Classify this cell by malaria status.
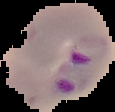

It is parasitized.

From a thin blood smear. Image is 115×112 pixels. Cell region segmented out of the field of view; the surrounding area is masked to black.